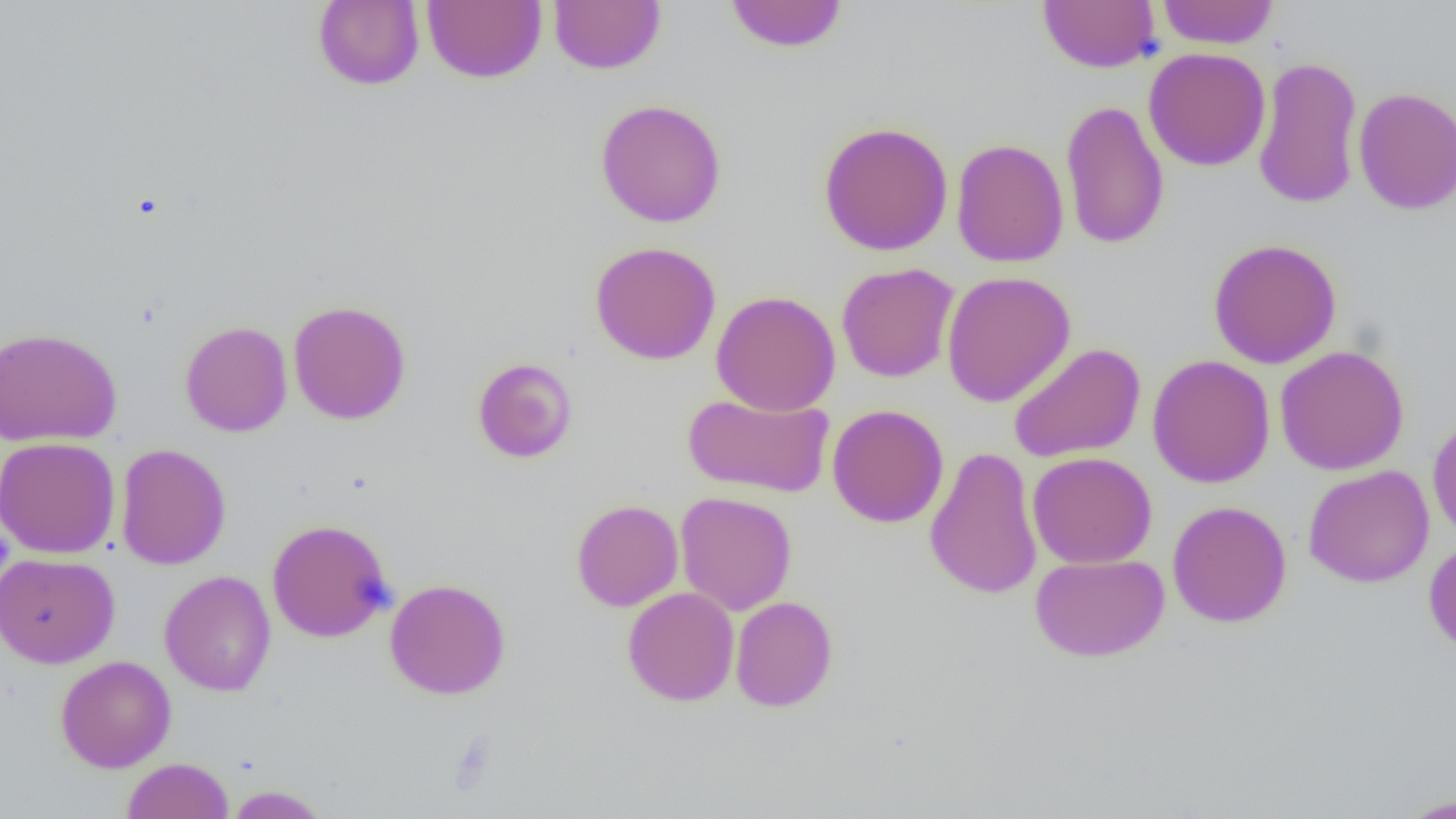
Summary:
  - Coordinate format: approximate bounding boxes as (x1,y1)-(x2,y2) corner pairs in pixels
  - Uninfected red blood cell locations: (313,0)-(425,90), (548,0)-(665,75), (723,0)-(849,53), (1037,0)-(1160,73), (1156,0)-(1279,49), (422,1)-(547,84), (1143,47)-(1271,171), (1252,54)-(1363,210), (1353,86)-(1456,215), (594,99)-(727,228), (1059,99)-(1169,251), (818,121)-(954,256), (950,138)-(1069,267), (1207,238)-(1342,368), (589,241)-(721,365), (836,263)-(959,383), (941,270)-(1076,407), (711,291)-(841,415), (288,299)-(411,425), (180,321)-(292,437), (0,327)-(122,446), (1008,342)-(1146,463), (1274,345)-(1409,476), (1147,354)-(1276,488), (473,357)-(578,463), (682,391)-(834,498), (826,404)-(949,528), (1427,416)-(1456,542), (0,437)-(120,558), (115,443)-(231,570), (924,446)-(1043,600), (1027,451)-(1157,569), (1303,465)-(1435,588), (675,491)-(797,615), (571,499)-(683,611), (1167,501)-(1292,627), (267,518)-(394,643), (1423,539)-(1456,654), (0,552)-(120,668), (1030,553)-(1169,661), (159,570)-(276,696), (384,578)-(511,699), (622,587)-(739,706), (730,595)-(838,712), (56,655)-(176,773), (122,757)-(233,819), (225,785)-(329,818), (1396,793)-(1455,818)
  - Slide-level diagnosis: no evidence of blood parasites
  - Field of view: one of a larger specimen
  - Modality: optical microscopy
  - Image size: 1456×819 pixels
  - Magnification: 1000x
  - Preparation: thin blood film